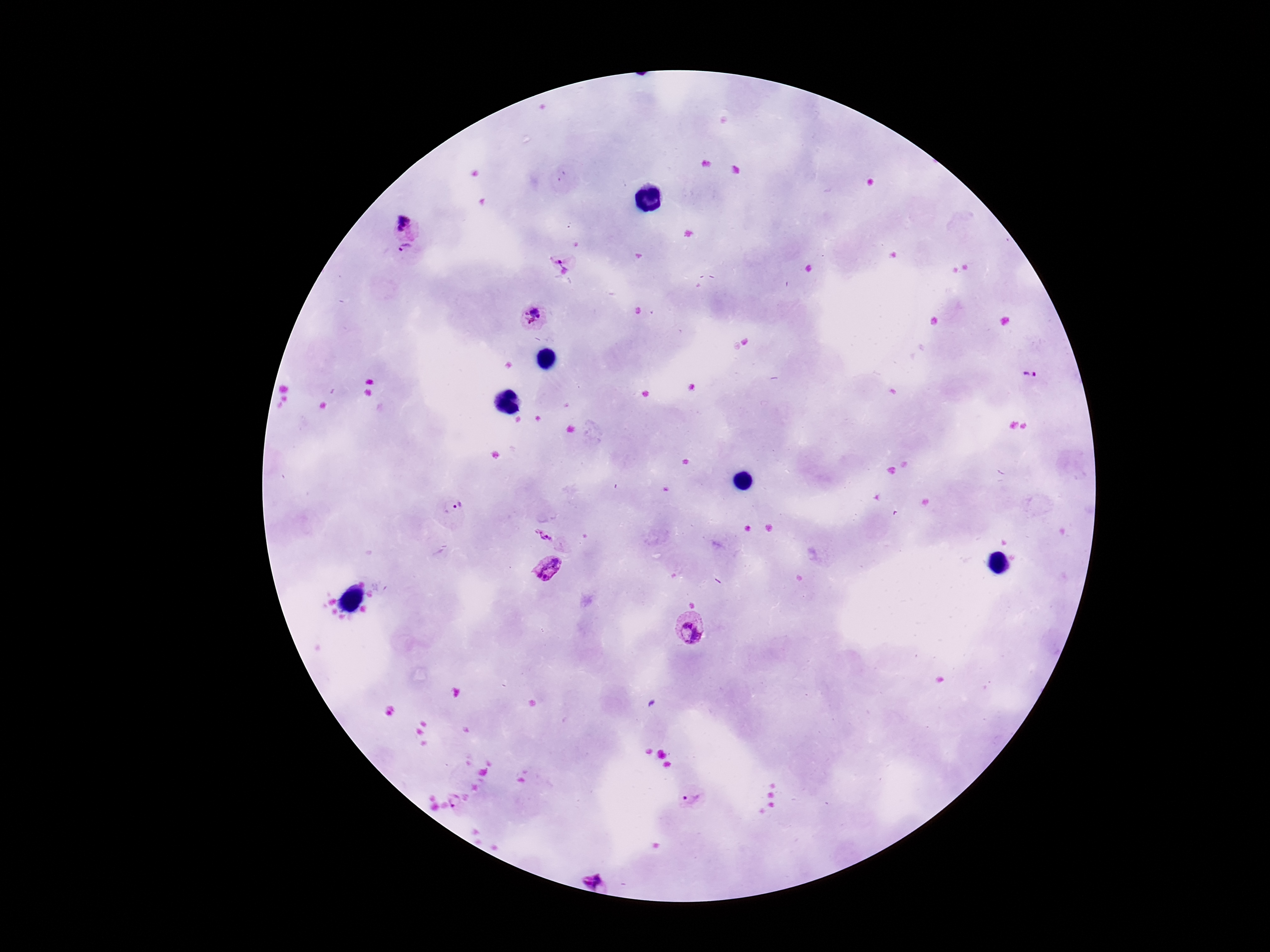
Approximate centers as (x, y) in pixels.
Summary:
  - Plasmodium parasite locations: (404, 228), (402, 258), (563, 265), (534, 317), (1029, 378), (454, 507), (543, 535), (549, 570), (692, 628), (692, 799), (455, 801), (595, 880)
  - Stain: Giemsa
  - Capture: smartphone camera through the microscope eyepiece
  - Field of view: one from this slide
  - Image size: 1270×952 pixels
  - Patient malaria status: positive
  - Preparation: thick peripheral-blood smear
  - Magnification: 100x